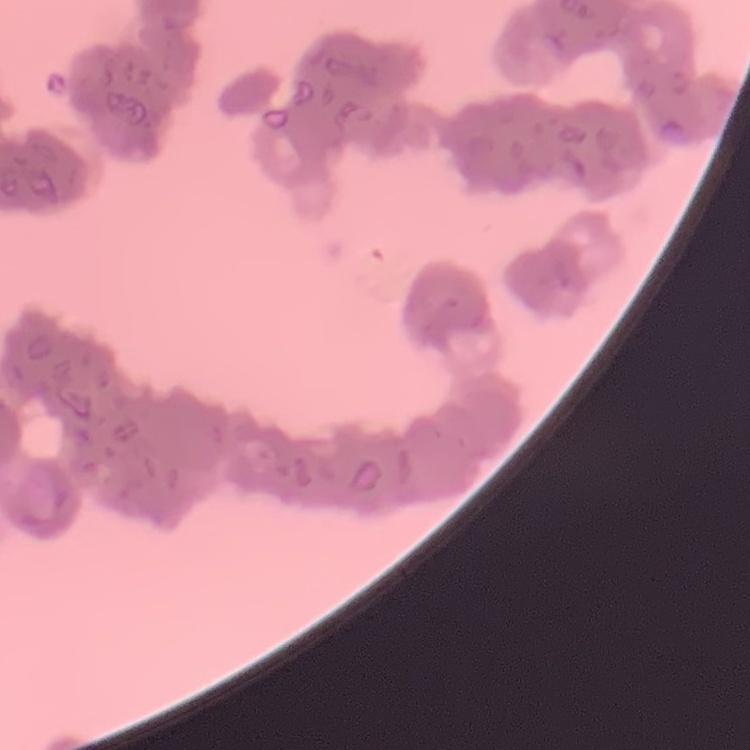
erythrocyte morphology = rouleaux formation
image type = square crop of a larger photomicrograph
stain = Field's or Giemsa
preparation = thin blood film